State the preparation type.
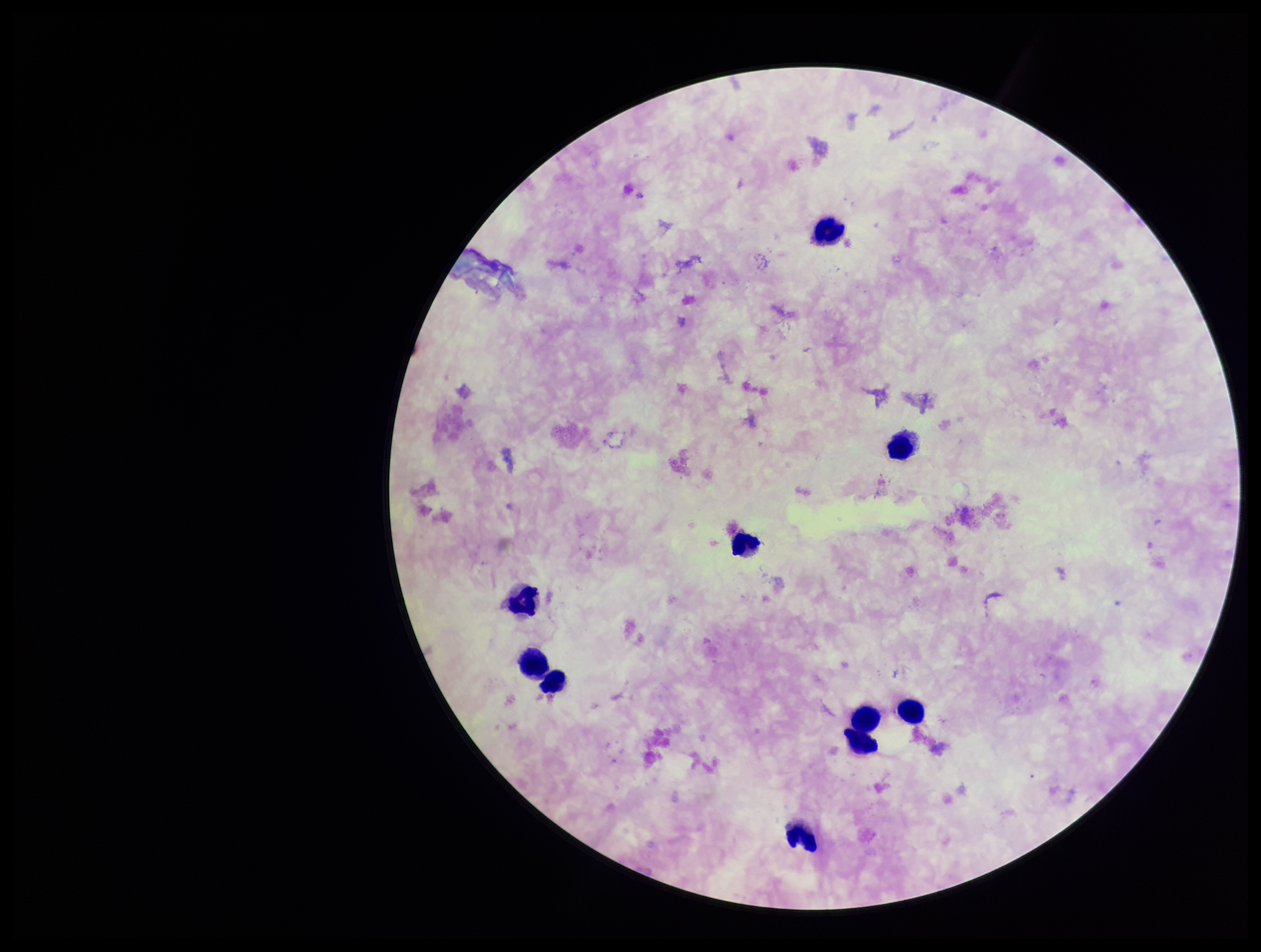
A thick smear.

Summary:
  - Species reported for this patient: Plasmodium falciparum
  - Plasmodium parasites: none detected
  - Field of view: single
  - Leukocyte count: 10
  - Capture: smartphone photograph through the microscope eyepiece
  - Parasite count: 0
  - Patient malaria status: infected
  - Stain: Giemsa
  - Image size: 1261×952 pixels